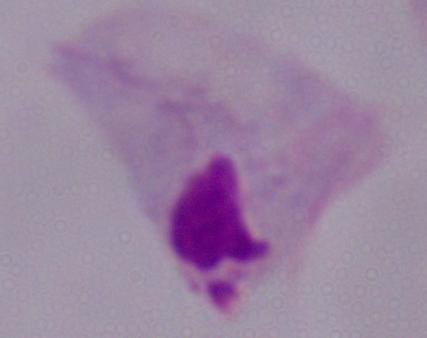
Summary:
  - Magnification: 1000x
  - Identification: trichomonad
  - Modality: photomicrograph